Outline each Babesia divergens-infected red blood cell.
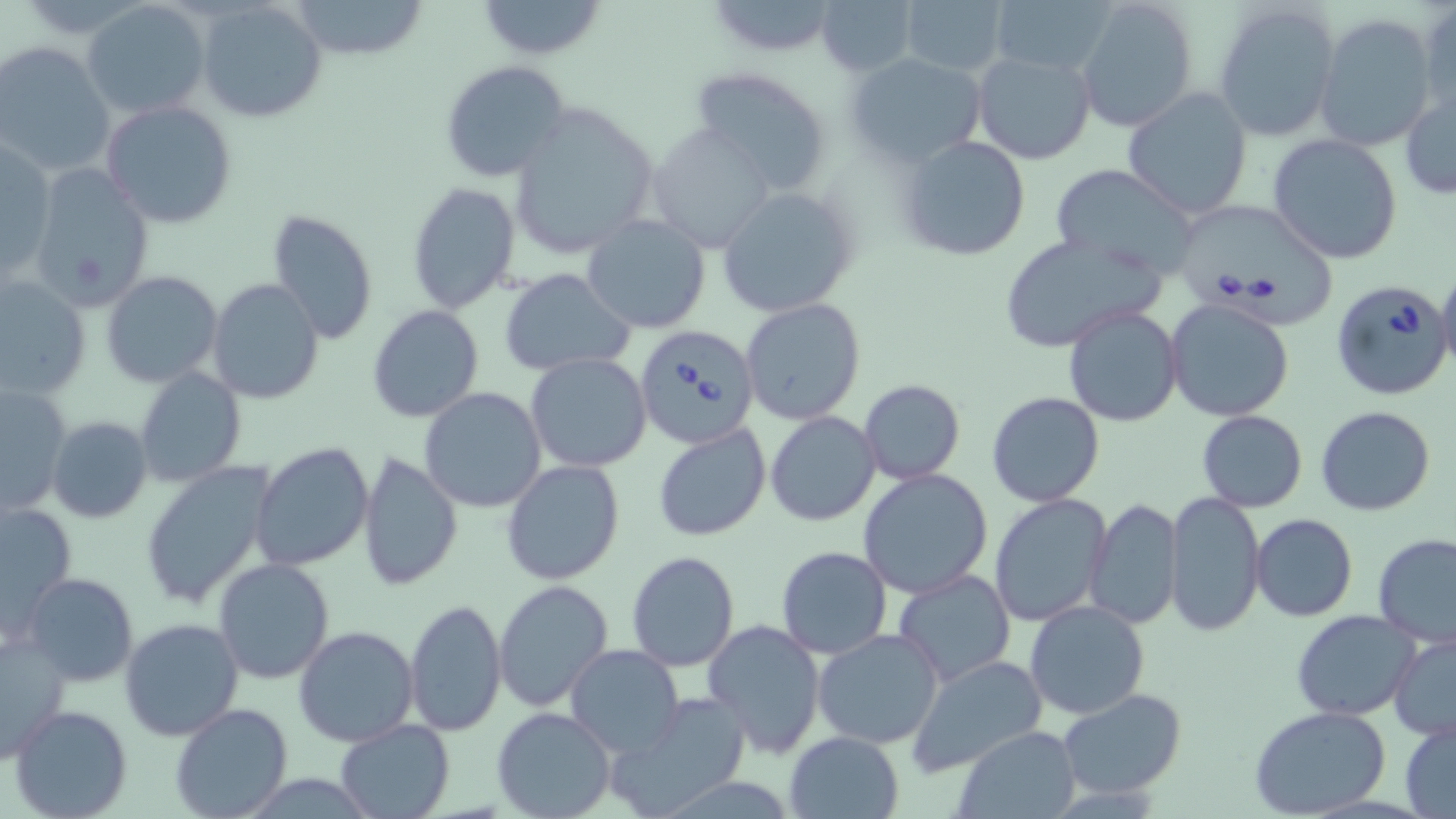
Approximate bounding boxes as (x1, y1, x2, y2) in pixels.
Babesia divergens-infected red blood cells: (1180, 204, 1338, 331), (1331, 279, 1456, 401), (634, 325, 760, 450).

Summary:
  - Uninfected red blood cell locations: (196, 0, 329, 122), (474, 0, 608, 60), (703, 0, 844, 58), (1074, 0, 1200, 133), (81, 1, 211, 119), (287, 1, 429, 59), (816, 1, 918, 76), (898, 1, 1010, 78), (988, 1, 1114, 79), (1213, 1, 1343, 143), (1418, 1, 1455, 124), (1314, 13, 1439, 153), (0, 42, 115, 179), (972, 49, 1098, 165), (845, 51, 989, 169), (441, 60, 570, 183), (689, 65, 835, 194), (1400, 86, 1456, 200), (1122, 88, 1254, 220), (101, 99, 238, 229), (507, 99, 661, 260), (647, 127, 778, 253), (896, 134, 1032, 261), (1268, 134, 1402, 264), (0, 141, 56, 278), (24, 162, 155, 313), (1047, 163, 1203, 277), (407, 182, 522, 316), (716, 184, 857, 319), (266, 209, 380, 345), (583, 214, 710, 334), (998, 230, 1162, 352), (1436, 263, 1456, 377), (501, 269, 636, 376), (102, 270, 222, 388), (1, 271, 91, 402), (207, 278, 326, 405), (740, 299, 867, 427), (1164, 299, 1296, 422), (367, 304, 484, 422), (1063, 304, 1183, 427), (526, 354, 653, 473), (134, 367, 247, 486), (859, 379, 965, 485), (0, 385, 73, 512), (419, 387, 548, 514), (987, 392, 1106, 508), (1316, 405, 1436, 516), (766, 411, 881, 527), (1196, 411, 1308, 512), (46, 416, 152, 523), (652, 422, 772, 541), (251, 441, 375, 573), (357, 452, 462, 592), (502, 459, 625, 584), (139, 460, 276, 612), (859, 468, 994, 598), (1164, 491, 1265, 637), (988, 495, 1112, 628), (1085, 499, 1182, 631), (1, 500, 77, 635), (1250, 513, 1358, 622), (1373, 532, 1456, 647), (775, 547, 892, 660), (626, 550, 741, 672), (213, 558, 337, 684), (893, 568, 1017, 685), (23, 573, 140, 686), (494, 578, 614, 711), (405, 598, 506, 736), (1025, 599, 1149, 720), (1291, 609, 1423, 721), (118, 616, 244, 741), (702, 619, 827, 756), (294, 626, 420, 747), (813, 627, 945, 749), (0, 629, 72, 762), (1388, 633, 1456, 741), (565, 645, 685, 757), (907, 653, 1049, 775), (1057, 689, 1187, 799), (606, 693, 750, 817), (170, 703, 293, 819), (9, 704, 132, 819), (1249, 704, 1395, 818), (491, 706, 616, 819), (333, 719, 454, 819), (1401, 719, 1456, 817), (951, 726, 1081, 818), (784, 731, 906, 818)
  - Slide-level diagnosis: Babesia divergens
  - Preparation: thin blood film
  - Modality: optical microscopy
  - Field of view: single
  - Image size: 1456×819 pixels
  - Stain: May-Grünwald-Giemsa
  - Magnification: 1000x